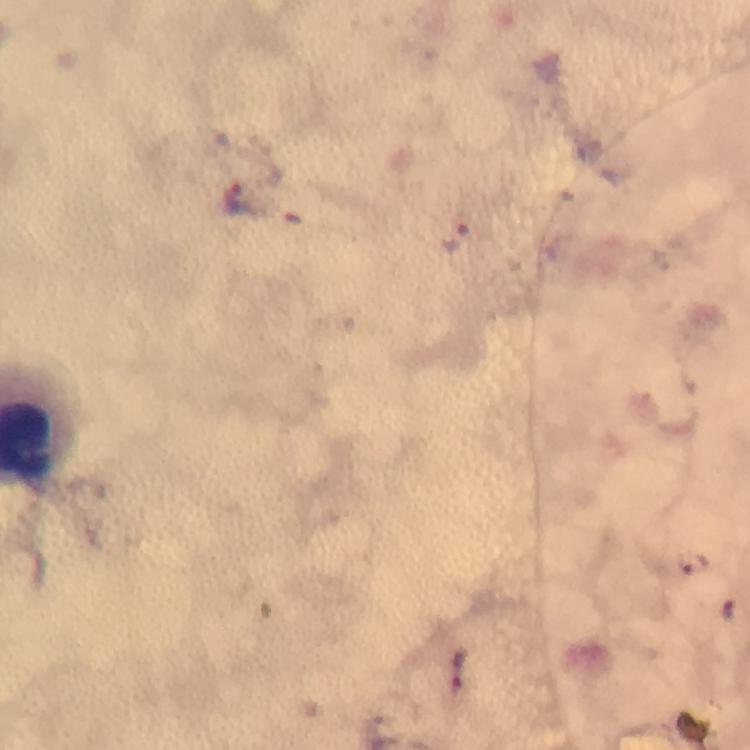
Approximate centers as {x, y} in pixels. Malaria parasite locations: {237, 197}, {455, 238}, {692, 562}, {730, 611}. At 100x magnification. Giemsa stain. Thick smear. Immersion oil was used. A crop from one field of view. From a diagnostic examination for malaria. Photographed with a smartphone mounted on the microscope. Image is 750×750 pixels.